Describe the morphology of the erythrocytes.
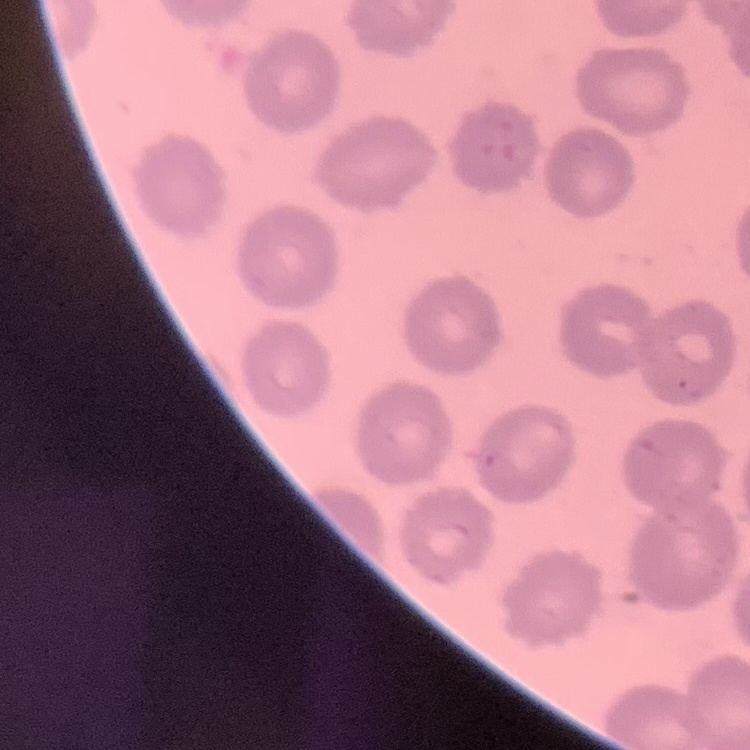
They show no rouleaux formation.

preparation = thin peripheral smear
stain = Field's or Giemsa
image type = square crop of a larger photomicrograph